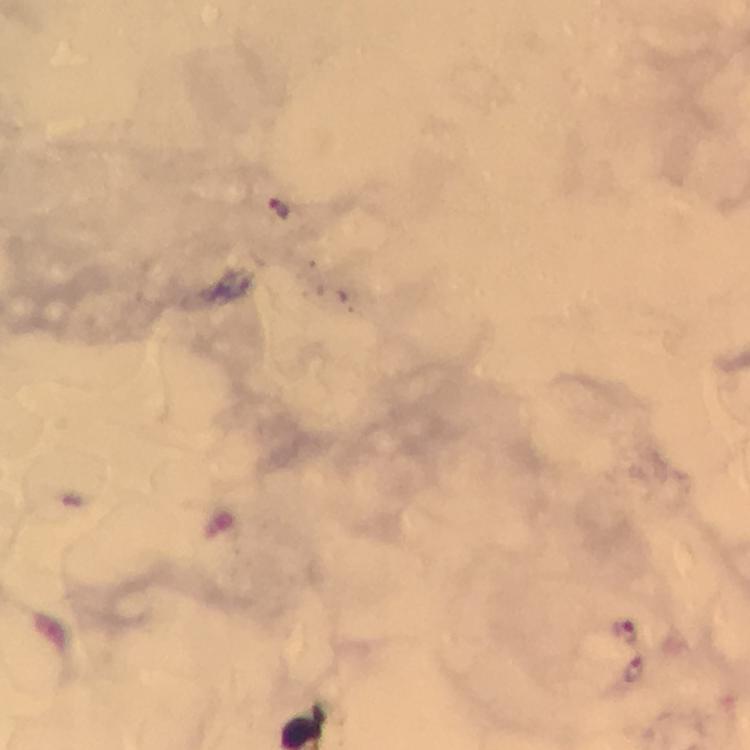

Approximate centers as (x, y) in pixels. Malaria parasite locations: (625, 630), (635, 670). Immersion oil was used. At 100x magnification. Photographed through the microscope with a smartphone camera. From a malaria diagnostic workup. Thick blood film. Image is 750×750 pixels. Giemsa stain. Cropped region of a single field of view.